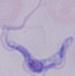

magnification = 1000x
identification = trypanosome
modality = photomicrograph